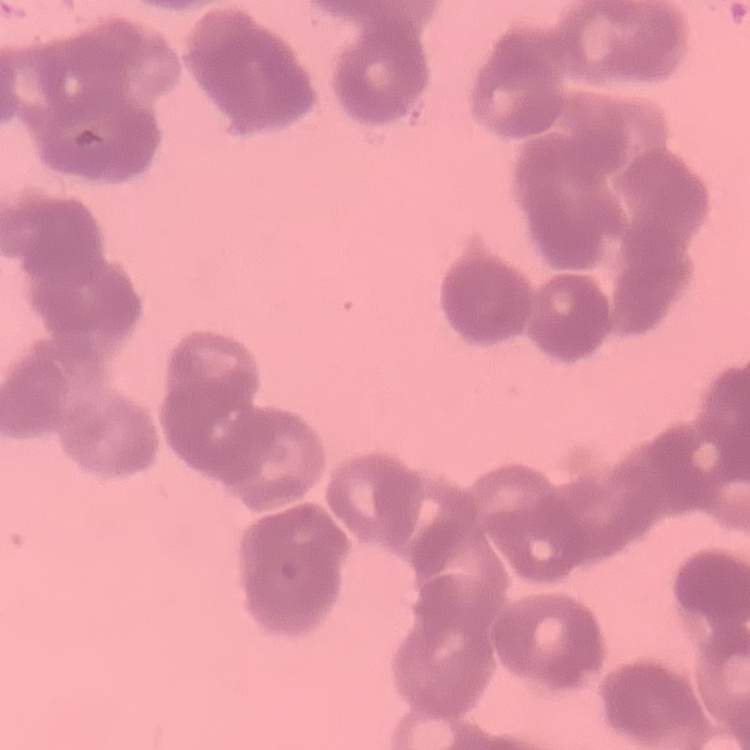
erythrocyte morphology = rouleaux formation
preparation = thin blood film
image type = one tile cut from a larger photomicrograph
stain = Field's or Giemsa